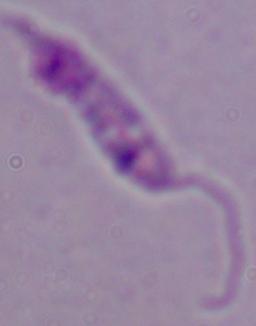

{
  "identification": "Leishmania",
  "magnification": "1000x",
  "modality": "micrograph"
}